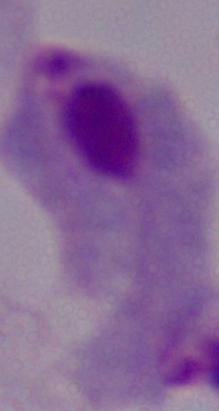
Summary:
  - Magnification: 1000x
  - Identification: trichomonad
  - Modality: micrograph